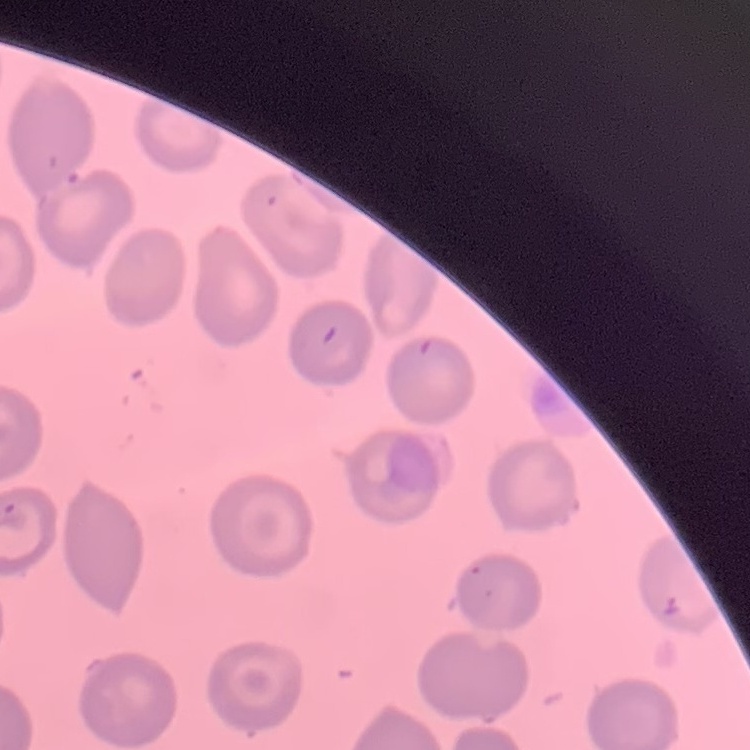 The red blood cells show no rouleaux formation. One tile cut from a larger photomicrograph. Thin blood film. Field's or Giemsa stain.